Outline each blood parasite and name the species.
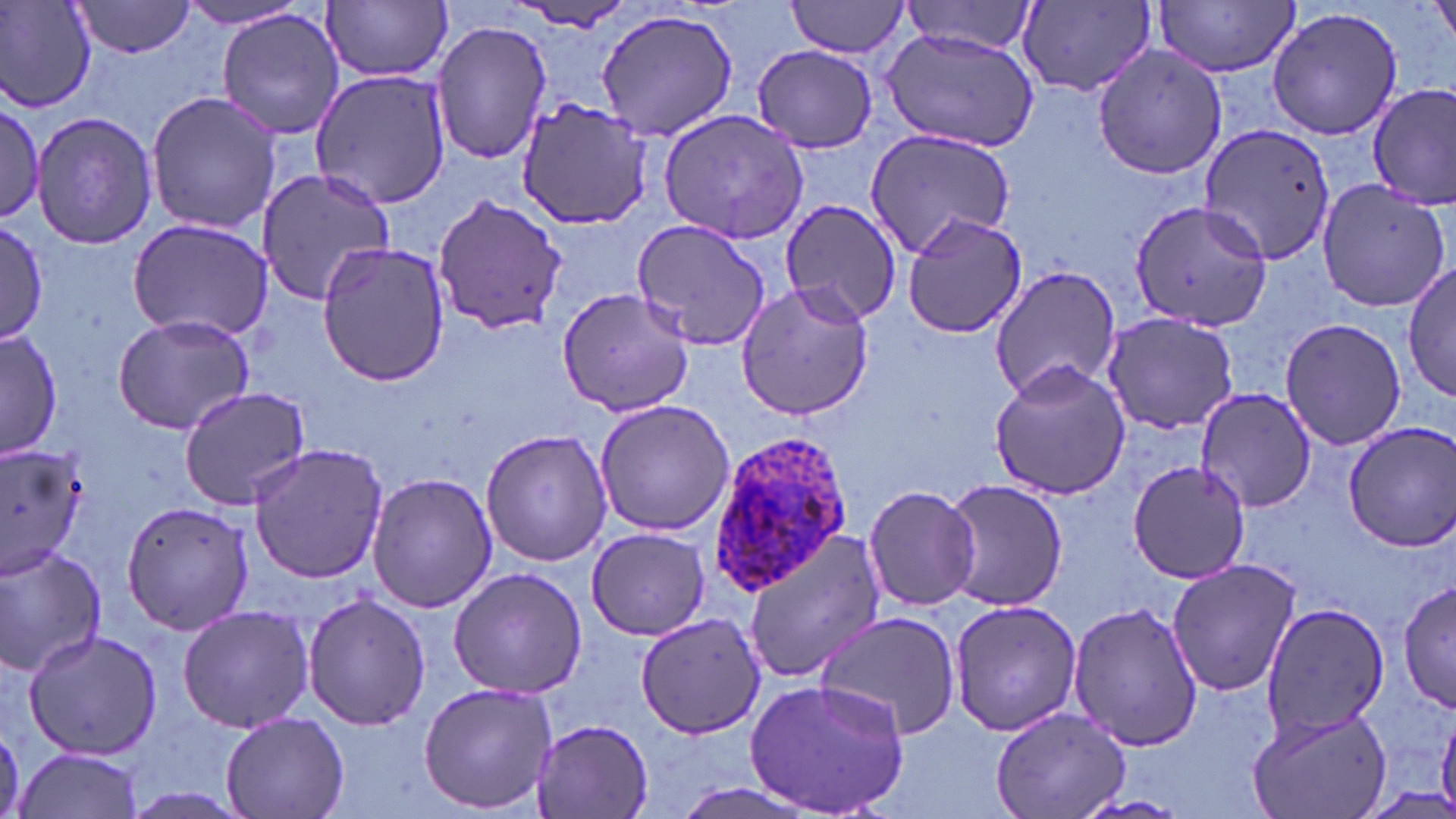

Approximate bounding boxes as named x1/y1/x2/y2 corners in pixels.
Plasmodium ovale-infected red blood cells: (x1=703, y1=434, x2=854, y2=592).
No Plasmodium falciparum, Plasmodium malariae, Plasmodium vivax, Babesia divergens, or Trypanosoma brucei observed.

Uninfected red blood cell locations: (x1=2, y1=0, x2=96, y2=113), (x1=68, y1=0, x2=196, y2=58), (x1=786, y1=0, x2=912, y2=58), (x1=1153, y1=0, x2=1300, y2=77), (x1=323, y1=1, x2=452, y2=83), (x1=901, y1=1, x2=1039, y2=56), (x1=1017, y1=1, x2=1156, y2=97), (x1=174, y1=3, x2=314, y2=31), (x1=502, y1=5, x2=642, y2=32), (x1=1267, y1=6, x2=1404, y2=140), (x1=592, y1=7, x2=741, y2=143), (x1=216, y1=8, x2=346, y2=140), (x1=430, y1=18, x2=553, y2=165), (x1=882, y1=29, x2=1040, y2=150), (x1=1090, y1=42, x2=1231, y2=181), (x1=753, y1=45, x2=882, y2=152), (x1=311, y1=57, x2=453, y2=212), (x1=1371, y1=84, x2=1456, y2=205), (x1=145, y1=89, x2=281, y2=235), (x1=0, y1=97, x2=54, y2=231), (x1=516, y1=100, x2=657, y2=229), (x1=658, y1=107, x2=813, y2=245), (x1=32, y1=110, x2=157, y2=250), (x1=1199, y1=123, x2=1336, y2=266), (x1=863, y1=128, x2=1015, y2=260), (x1=254, y1=166, x2=396, y2=306), (x1=1314, y1=178, x2=1452, y2=314), (x1=431, y1=194, x2=565, y2=336), (x1=778, y1=197, x2=903, y2=326), (x1=1128, y1=199, x2=1275, y2=332), (x1=898, y1=209, x2=1029, y2=336), (x1=0, y1=212, x2=48, y2=349), (x1=128, y1=218, x2=274, y2=340), (x1=630, y1=218, x2=777, y2=352), (x1=317, y1=239, x2=449, y2=387), (x1=1404, y1=262, x2=1455, y2=405), (x1=987, y1=266, x2=1125, y2=401), (x1=734, y1=280, x2=877, y2=421), (x1=556, y1=284, x2=697, y2=418), (x1=1101, y1=311, x2=1242, y2=434), (x1=112, y1=313, x2=255, y2=435), (x1=1280, y1=315, x2=1406, y2=451), (x1=2, y1=329, x2=62, y2=458), (x1=988, y1=360, x2=1131, y2=500), (x1=177, y1=384, x2=311, y2=510), (x1=1197, y1=388, x2=1317, y2=512), (x1=593, y1=398, x2=735, y2=538), (x1=1341, y1=422, x2=1456, y2=551), (x1=480, y1=427, x2=613, y2=567), (x1=0, y1=441, x2=88, y2=580), (x1=246, y1=444, x2=389, y2=584), (x1=1127, y1=460, x2=1250, y2=585), (x1=366, y1=472, x2=497, y2=614), (x1=942, y1=477, x2=1068, y2=612), (x1=862, y1=484, x2=981, y2=612), (x1=121, y1=501, x2=257, y2=636), (x1=586, y1=526, x2=709, y2=640), (x1=738, y1=531, x2=886, y2=685), (x1=0, y1=543, x2=107, y2=677), (x1=1163, y1=558, x2=1301, y2=696), (x1=448, y1=567, x2=588, y2=699), (x1=1396, y1=576, x2=1456, y2=712), (x1=301, y1=592, x2=432, y2=732), (x1=947, y1=598, x2=1084, y2=737), (x1=1065, y1=599, x2=1203, y2=752), (x1=1259, y1=602, x2=1390, y2=736), (x1=177, y1=605, x2=315, y2=734), (x1=812, y1=611, x2=963, y2=738), (x1=636, y1=614, x2=768, y2=739), (x1=22, y1=631, x2=163, y2=761), (x1=417, y1=680, x2=558, y2=814), (x1=744, y1=680, x2=912, y2=817), (x1=1245, y1=705, x2=1392, y2=819), (x1=991, y1=706, x2=1132, y2=819), (x1=221, y1=710, x2=349, y2=819), (x1=528, y1=719, x2=656, y2=817), (x1=14, y1=746, x2=144, y2=819). Slide-level diagnosis: Plasmodium ovale. Image is 1456×819 pixels. Captured at 1000x magnification. One field of a larger specimen. May-Grünwald-Giemsa stain. Light microscopy. Thin blood smear.